Name the parasite shown.
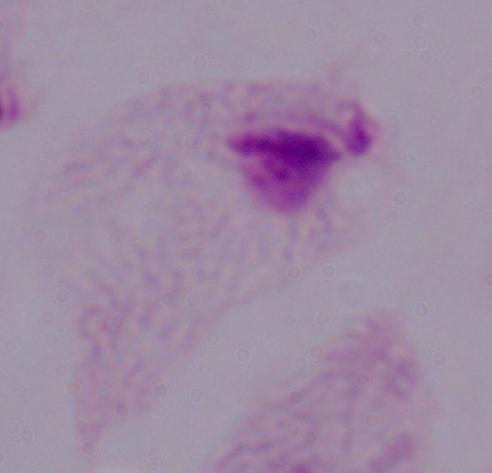
A trichomonad.

Summary:
  - Modality: photomicrograph
  - Magnification: 1000x